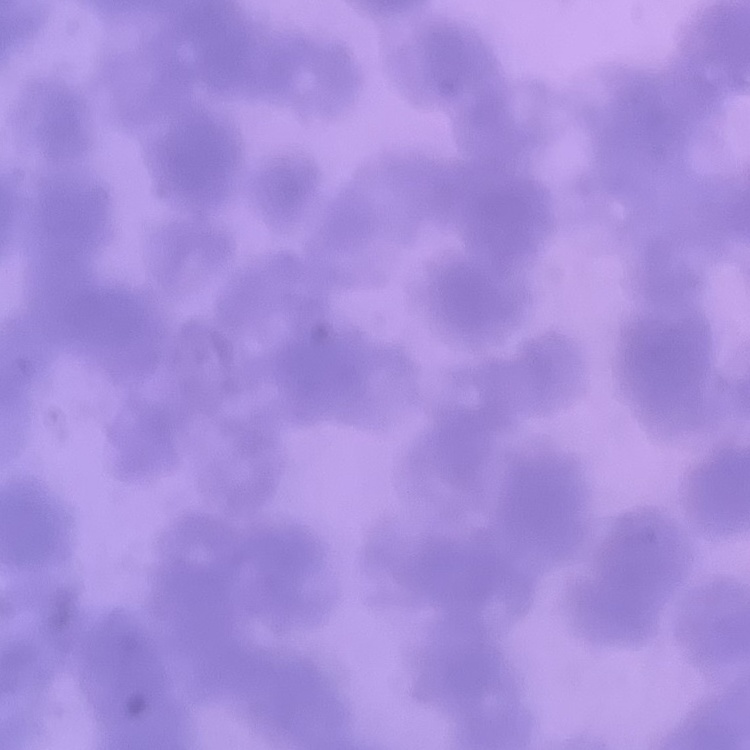

Summary:
  - Erythrocyte morphology: rouleaux formation
  - Preparation: thin peripheral smear
  - Image type: square crop of a larger photomicrograph
  - Stain: Field's or Giemsa